Locate and identify every blood parasite.
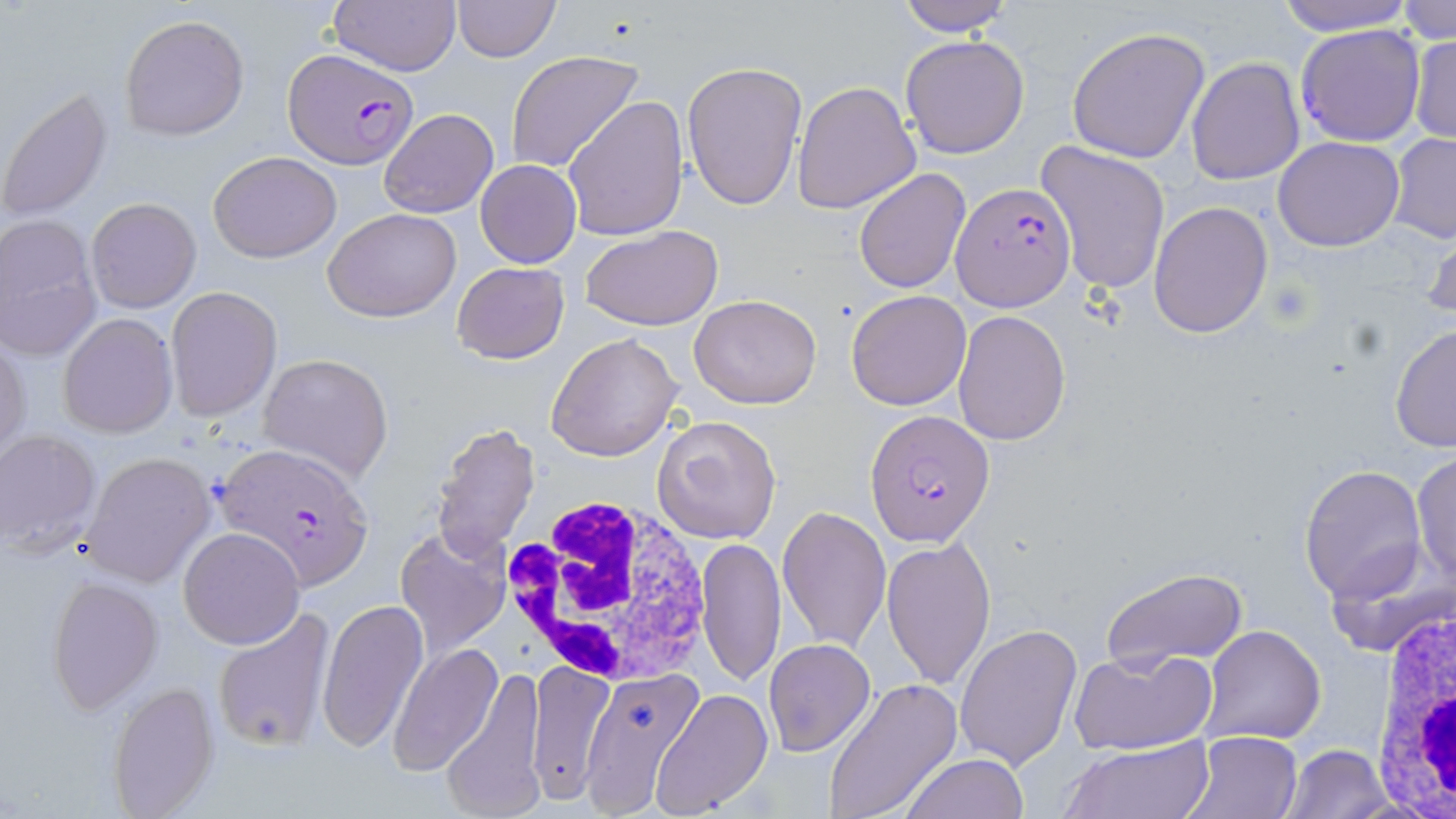
Approximate bounding boxes as [x1, y1, x2, y2] in pixels.
Plasmodium falciparum-infected red blood cells: [1294, 23, 1426, 147], [285, 50, 418, 167], [951, 181, 1076, 310], [865, 408, 992, 547], [215, 441, 376, 590].
No Plasmodium ovale, Plasmodium malariae, Plasmodium vivax, Babesia divergens, or Trypanosoma brucei observed.

{
  "slide_level_diagnosis": "Plasmodium falciparum",
  "platelet_locations": "approximate bounding boxes as [x1, y1, x2, y2] in pixels: [1265, 279, 1314, 327]",
  "field_of_view": "one of a larger specimen",
  "image_size": "1456×819 pixels",
  "preparation": "thin blood smear",
  "uninfected_red_blood_cell_locations": "approximate bounding boxes as [x1, y1, x2, y2] in pixels: [327, 0, 462, 76], [452, 0, 560, 62], [893, 0, 1016, 37], [1271, 0, 1418, 36], [1396, 2, 1456, 44], [119, 13, 249, 141], [1066, 26, 1211, 163], [900, 34, 1031, 158], [1408, 34, 1456, 146], [506, 49, 645, 174], [1186, 57, 1305, 186], [682, 61, 807, 210], [569, 78, 804, 223], [792, 80, 920, 214], [1, 86, 113, 222], [563, 95, 690, 241], [378, 108, 498, 219], [1388, 132, 1455, 244], [1273, 137, 1404, 252], [1034, 141, 1170, 296], [209, 150, 341, 263], [476, 159, 581, 268], [853, 168, 971, 294], [85, 198, 202, 314], [1148, 201, 1273, 339], [324, 208, 461, 323], [0, 217, 102, 361], [1420, 219, 1456, 327], [580, 223, 723, 330], [451, 261, 570, 364], [166, 287, 282, 420], [845, 289, 972, 411], [689, 294, 822, 408], [953, 311, 1071, 446], [58, 312, 177, 439], [1388, 324, 1456, 453], [547, 332, 681, 463], [0, 335, 30, 459], [259, 351, 394, 481], [652, 412, 783, 546], [429, 420, 542, 562], [0, 429, 101, 556], [1410, 452, 1456, 587], [81, 453, 213, 586], [1300, 466, 1427, 600], [776, 504, 890, 655], [178, 527, 305, 649], [396, 527, 511, 658], [696, 536, 786, 687], [881, 537, 997, 690], [1102, 567, 1248, 670], [45, 575, 163, 714], [316, 597, 430, 753], [213, 608, 336, 751], [954, 623, 1082, 769], [1204, 626, 1325, 745], [764, 638, 876, 755], [389, 641, 503, 777], [1071, 648, 1215, 756], [527, 660, 615, 804], [441, 663, 547, 819], [579, 670, 706, 819], [823, 677, 963, 819], [107, 682, 219, 816], [651, 689, 773, 818], [1182, 729, 1303, 819], [1060, 737, 1214, 819], [1282, 743, 1394, 818], [901, 753, 1028, 819]",
  "magnification": "1000x",
  "stain": "May-Grünwald-Giemsa",
  "modality": "optical microscopy",
  "white_blood_cell_locations": "approximate bounding boxes as [x1, y1, x2, y2] in pixels: [502, 489, 720, 687], [1365, 586, 1456, 819]"
}